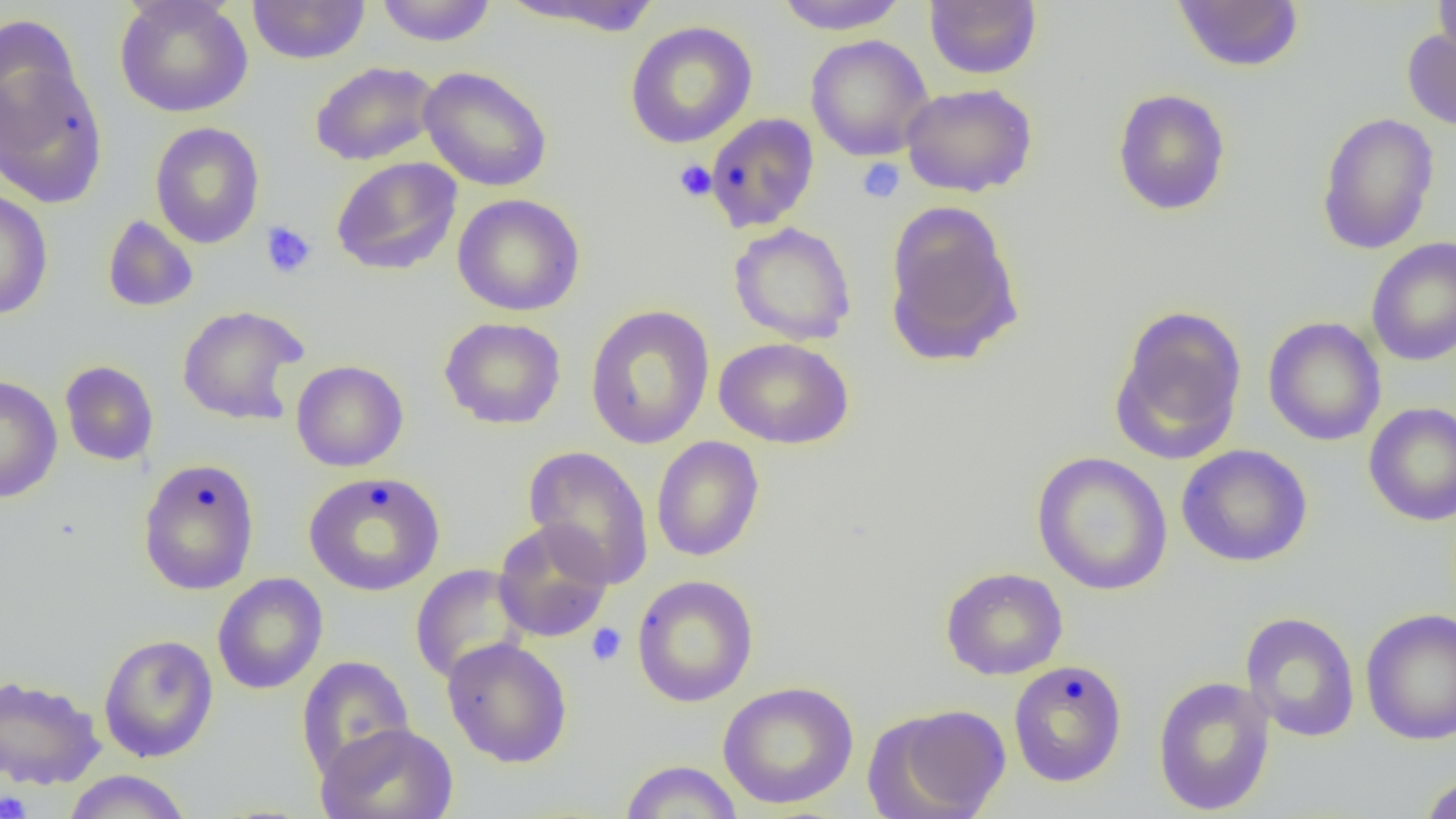
Summary:
  - Coordinate format: approximate bounding boxes as (x1,y1)-(x2,y2) corner pairs in pixels
  - Uninfected red blood cell locations: (115,0)-(253,118), (247,0)-(370,65), (375,0)-(497,47), (500,0)-(666,36), (772,0)-(910,34), (924,0)-(1042,80), (1172,0)-(1304,73), (1432,0)-(1456,65), (0,13)-(84,143), (625,20)-(758,149), (1402,26)-(1456,132), (805,35)-(934,161), (0,57)-(109,208), (310,61)-(441,166), (418,66)-(553,192), (900,83)-(1037,197), (1112,88)-(1231,216), (1316,112)-(1440,255), (705,113)-(819,233), (150,121)-(265,249), (331,157)-(462,276), (0,188)-(54,320), (452,194)-(585,316), (884,201)-(1023,366), (102,215)-(199,312), (728,222)-(857,345), (1365,237)-(1456,366), (584,304)-(715,450), (1109,304)-(1248,465), (177,305)-(308,425), (1262,316)-(1386,446), (440,317)-(566,429), (714,337)-(854,449), (291,360)-(409,472), (59,361)-(159,466), (0,375)-(63,503), (1363,402)-(1456,526), (651,436)-(765,562), (523,444)-(654,590), (1176,444)-(1313,567), (1031,451)-(1172,596), (138,457)-(260,595), (303,471)-(446,597), (493,520)-(614,643), (410,564)-(531,685), (940,567)-(1068,680), (212,573)-(328,695), (631,574)-(759,708), (1361,608)-(1456,745), (1241,611)-(1360,742), (98,634)-(219,762), (442,637)-(573,768), (296,655)-(414,781), (1008,660)-(1127,787), (0,674)-(106,790), (1152,675)-(1276,816), (717,681)-(859,809), (866,703)-(1012,819), (315,723)-(459,819), (618,759)-(744,818), (63,770)-(192,819), (1417,773)-(1456,819)
  - Platelet locations: (857,158)-(905,204), (673,159)-(716,202), (260,221)-(317,279), (586,623)-(628,667), (0,790)-(32,819)
  - Slide-level diagnosis: no evidence of blood parasites
  - Magnification: 1000x
  - Modality: optical microscopy
  - Image size: 1456×819 pixels
  - Field of view: single
  - Preparation: thin blood film